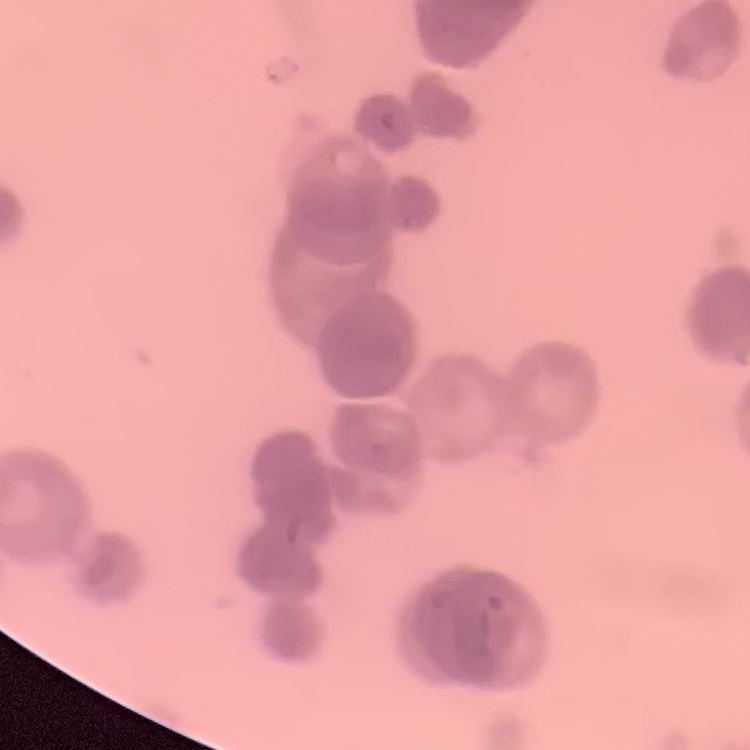
red blood cell morphology = rouleaux formation
image type = square crop of a larger photomicrograph
preparation = thin blood smear
stain = Field's or Giemsa